Assess this cell for malaria.
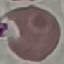

Uninfected.

Summary:
  - Stain: Giemsa
  - Image type: cell patch, automatically extracted from a larger field of view and resized to 64 × 64 pixels
  - Preparation: thin blood film
  - Capture: smartphone camera at the microscope eyepiece